Give the extent of all uninfected red blood cells.
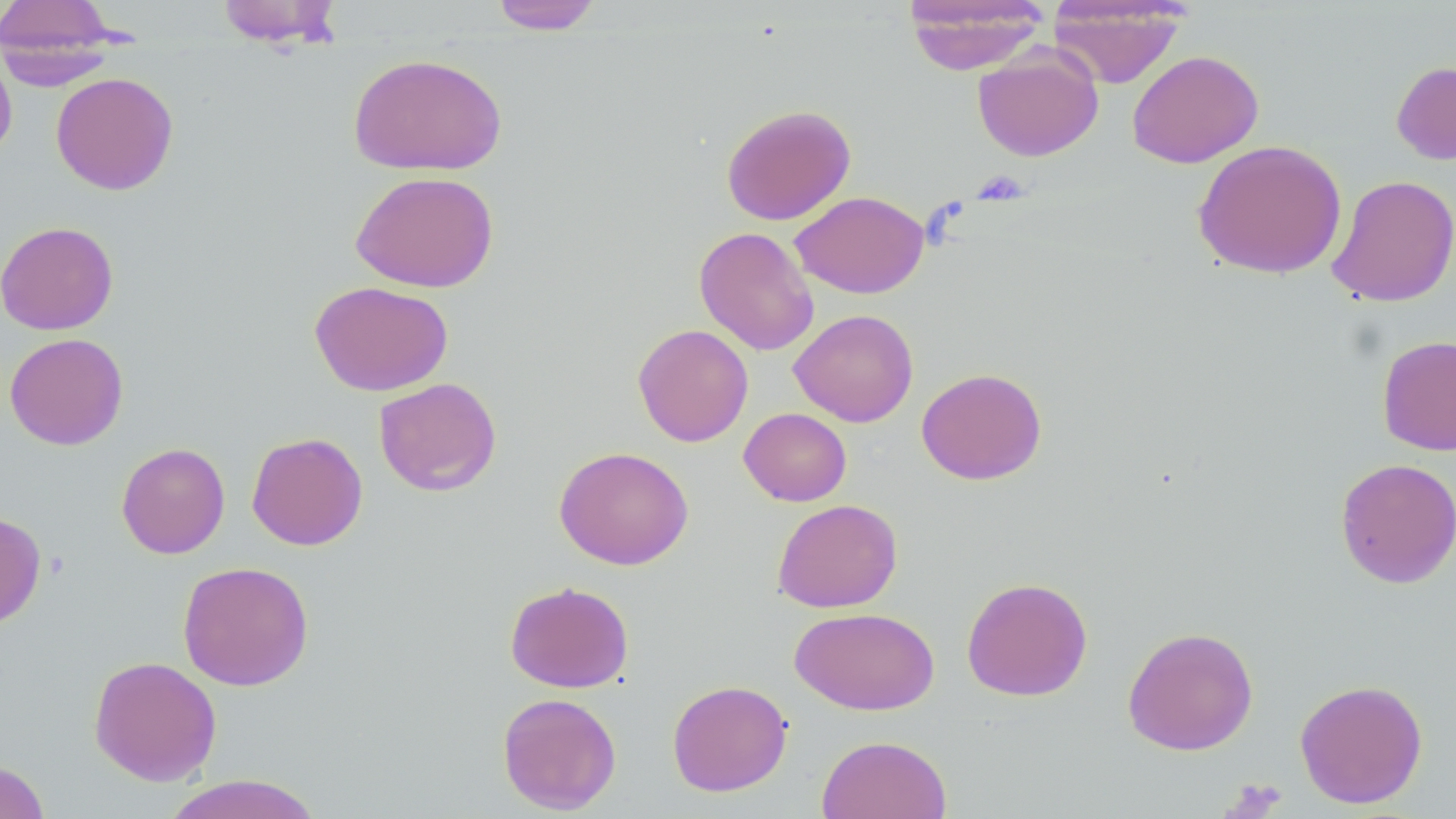
Approximate bounding boxes as (x1,y1)-(x2,y2) corner pairs in pixels.
Uninfected red blood cells: (215,0)-(344,47), (489,0)-(604,34), (903,0)-(1050,74), (0,1)-(123,80), (1048,1)-(1187,88), (0,44)-(17,161), (972,47)-(1103,162), (1126,50)-(1264,168), (347,52)-(508,177), (1391,60)-(1456,165), (51,72)-(179,195), (720,104)-(856,225), (1192,140)-(1347,280), (349,170)-(500,293), (1327,174)-(1456,308), (790,191)-(929,298), (0,221)-(119,335), (694,227)-(820,355), (309,280)-(453,396), (789,308)-(919,427), (632,323)-(754,447), (4,333)-(128,450), (1377,335)-(1456,456), (916,367)-(1047,485), (374,377)-(502,496), (739,407)-(851,506), (246,431)-(368,551), (116,442)-(230,559), (554,446)-(694,570), (1335,457)-(1456,589), (772,498)-(903,613), (0,511)-(47,630), (177,560)-(314,691), (961,576)-(1093,701), (504,580)-(634,693), (789,607)-(940,715), (1122,625)-(1259,756), (88,655)-(222,786), (1294,678)-(1429,808), (667,679)-(792,797), (496,692)-(622,815), (816,735)-(953,819), (1,759)-(50,819), (162,774)-(324,819).

Summary:
  - Platelet locations: (972,170)-(1031,204)
  - Slide-level diagnosis: negative for blood parasites
  - Magnification: 1000x
  - Image size: 1456×819 pixels
  - Field of view: single
  - Modality: optical microscopy
  - Preparation: thin blood film
  - Stain: May-Grünwald-Giemsa